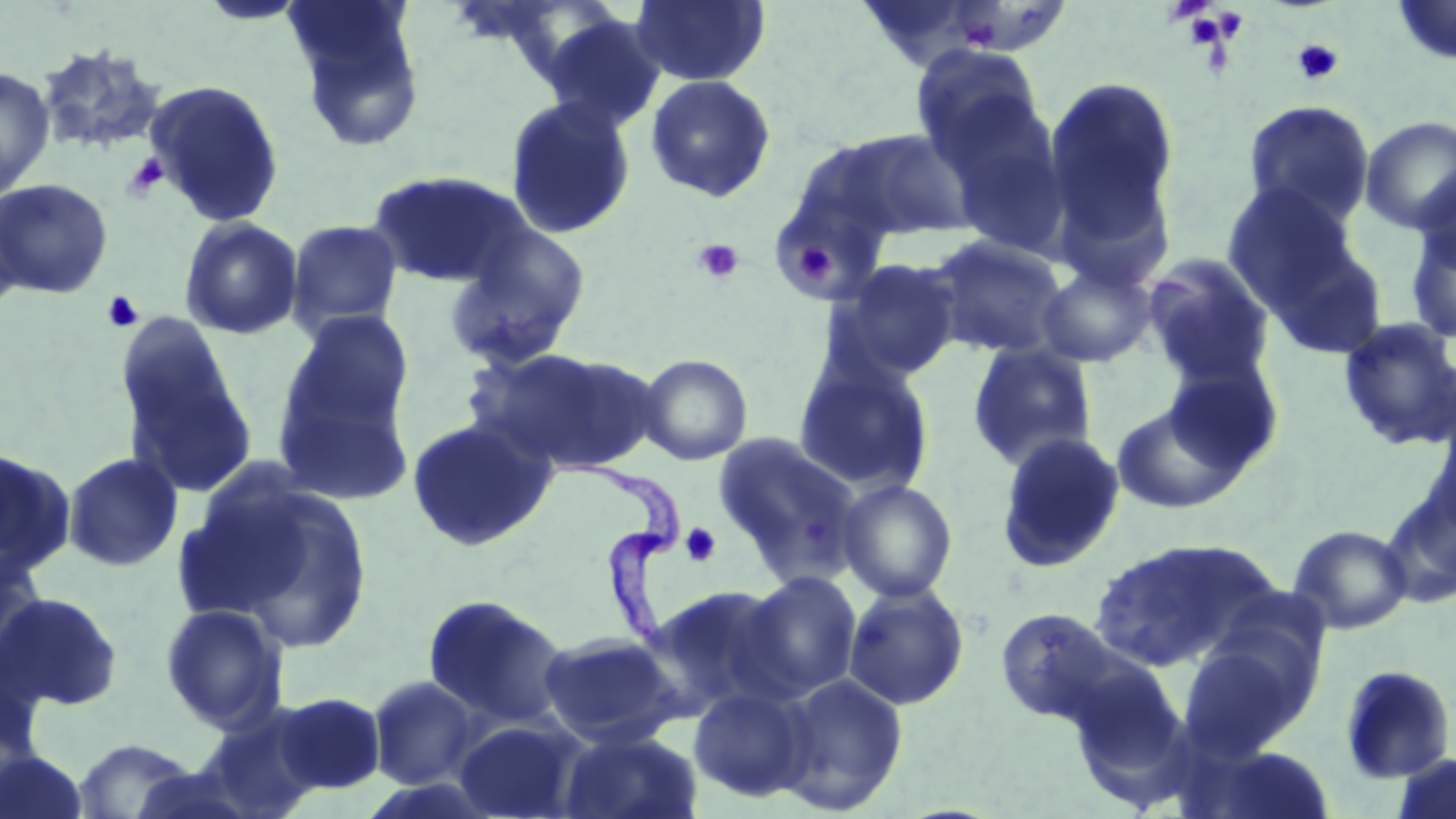 Approximate bounding boxes as (x1,y1)-(x2,y2) corner pairs in pixels. Platelet locations: (1183,13)-(1231,49), (1293,38)-(1345,86), (124,152)-(168,200), (692,238)-(744,283), (791,240)-(837,287), (102,290)-(145,333), (681,522)-(722,567). Uninfected red blood cell locations: (283,0)-(427,152), (630,0)-(771,87), (1391,0)-(1456,67), (539,13)-(667,134), (35,43)-(167,157), (909,45)-(1047,164), (0,66)-(55,197), (1043,74)-(1183,261), (644,75)-(777,203), (144,79)-(285,226), (504,96)-(637,239), (1243,99)-(1375,229), (936,101)-(1073,258), (1360,116)-(1456,235), (822,128)-(976,244), (366,168)-(531,288), (1413,168)-(1456,278), (0,178)-(114,298), (769,181)-(894,305), (1221,183)-(1362,313), (0,200)-(24,322), (179,216)-(304,340), (286,219)-(404,336), (1405,220)-(1456,346), (444,225)-(591,371), (927,235)-(1068,358), (1261,237)-(1390,362), (1142,254)-(1276,388), (829,258)-(965,380), (1035,263)-(1158,367), (282,309)-(414,439), (1337,317)-(1456,451), (119,327)-(256,498), (967,342)-(1098,470), (468,346)-(655,473), (638,353)-(753,465), (794,358)-(936,496), (1162,358)-(1285,476), (273,379)-(415,509), (1109,400)-(1248,514), (406,416)-(558,552), (995,431)-(1126,573), (713,433)-(863,580), (0,446)-(77,578), (62,452)-(183,572), (197,479)-(378,652), (838,479)-(959,602), (1381,485)-(1456,609), (1289,524)-(1412,634), (1091,538)-(1272,671), (0,546)-(49,671), (740,571)-(863,701), (843,584)-(970,710), (645,585)-(793,718), (0,591)-(123,711), (422,594)-(571,728), (159,603)-(289,732), (994,607)-(1125,728), (538,632)-(685,747), (1177,638)-(1313,756), (1064,661)-(1187,783), (1338,663)-(1456,784), (773,673)-(908,815), (367,675)-(480,789), (688,686)-(814,803), (270,691)-(386,796), (199,707)-(326,819), (454,719)-(585,818), (557,729)-(703,819), (71,737)-(199,818), (1185,742)-(1339,819), (0,749)-(89,819), (1391,753)-(1456,819). Trypanosoma brucei locations: (553,449)-(688,662). Slide-level diagnosis: Trypanosoma brucei. Optical microscopy. May-Grünwald-Giemsa-stained preparation. Single field of view. Image is 1456×819 pixels. Captured at 1000x magnification. Thin blood smear.